State which parasite is depicted.
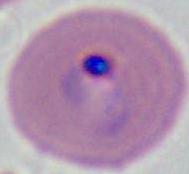
This is Plasmodium.

Captured at either 400x or 1000x magnification. Micrograph.